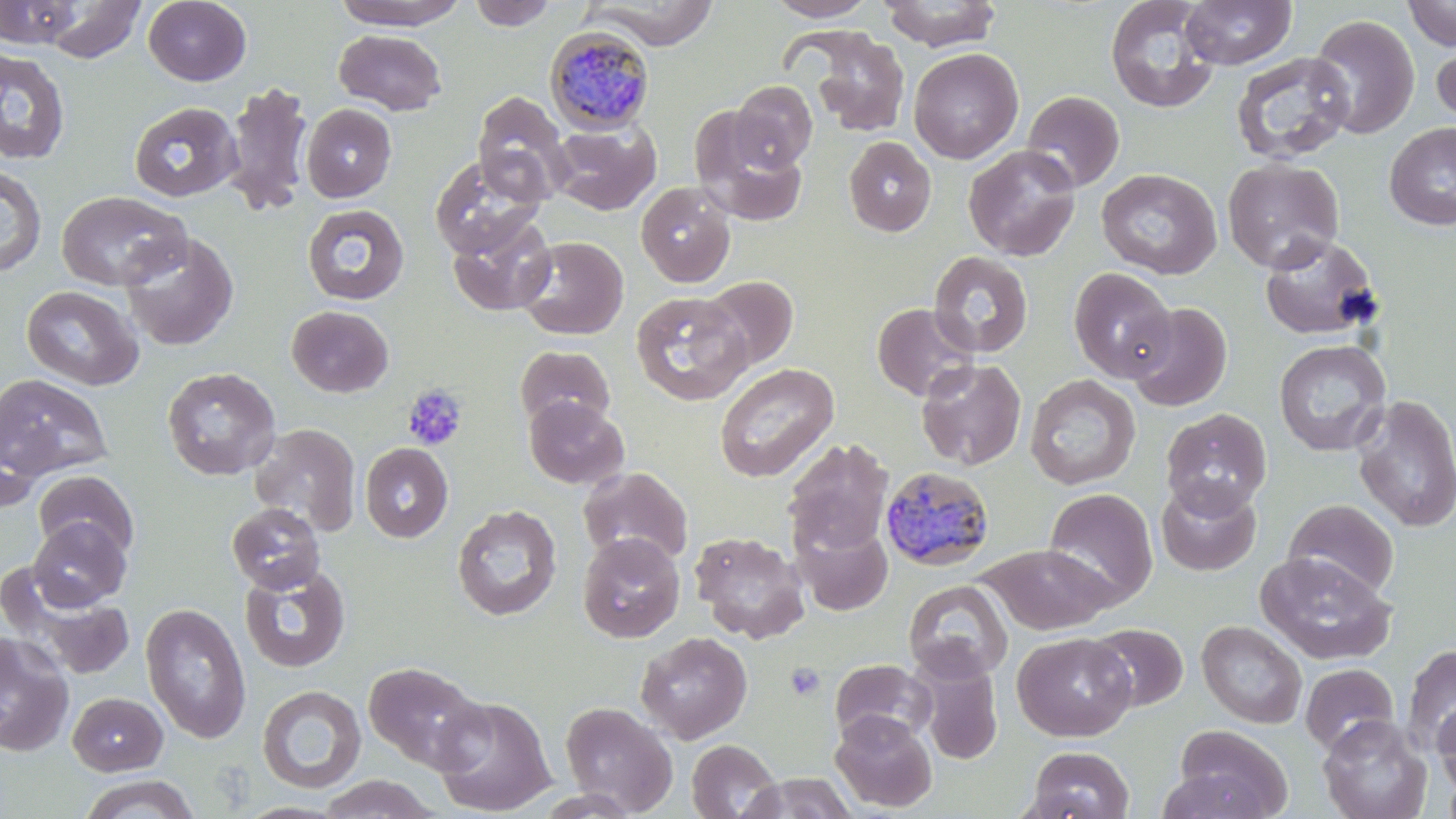
Approximate bounding boxes as [x1, y1, x2, y2] in pixels. Plasmodium malariae-infected red blood cell locations: [544, 26, 656, 134], [879, 465, 995, 571]. Platelet locations: [403, 384, 467, 450], [785, 662, 827, 701]. Uninfected red blood cell locations: [43, 0, 147, 63], [143, 0, 251, 86], [331, 0, 470, 29], [468, 0, 557, 30], [584, 0, 721, 48], [763, 0, 878, 21], [879, 0, 1003, 51], [1104, 0, 1220, 114], [1180, 0, 1296, 69], [0, 1, 84, 48], [1403, 1, 1456, 51], [1308, 14, 1420, 140], [796, 26, 912, 137], [333, 29, 447, 115], [1432, 36, 1456, 132], [0, 47, 71, 165], [909, 47, 1023, 164], [1230, 52, 1355, 165], [223, 81, 314, 216], [731, 81, 817, 171], [472, 90, 571, 203], [1021, 91, 1124, 192], [128, 101, 242, 202], [301, 103, 396, 202], [689, 108, 808, 226], [548, 122, 660, 215], [1384, 122, 1456, 230], [844, 136, 936, 237], [963, 144, 1082, 261], [429, 154, 545, 259], [1222, 158, 1344, 273], [0, 164, 47, 278], [1096, 168, 1222, 279], [635, 182, 736, 287], [56, 190, 190, 291], [302, 203, 410, 305], [446, 211, 556, 317], [120, 231, 239, 350], [1259, 232, 1381, 341], [516, 236, 628, 340], [928, 251, 1034, 358], [1068, 268, 1177, 383], [699, 276, 798, 372], [20, 285, 144, 390], [631, 291, 753, 406], [872, 302, 979, 402], [1125, 302, 1233, 412], [286, 305, 394, 398], [1273, 339, 1391, 457], [515, 345, 615, 432], [915, 358, 1026, 471], [713, 362, 839, 483], [161, 367, 281, 481], [0, 373, 113, 481], [1025, 374, 1141, 490], [1351, 395, 1456, 533], [523, 396, 629, 489], [1161, 407, 1272, 517], [0, 409, 44, 515], [249, 422, 361, 536], [783, 437, 894, 555], [361, 443, 453, 543], [578, 466, 693, 568], [33, 470, 139, 561], [1156, 479, 1261, 576], [1043, 487, 1158, 609], [1283, 499, 1399, 599], [227, 502, 326, 594], [452, 504, 562, 621], [27, 516, 131, 611], [793, 519, 893, 616], [689, 531, 809, 643], [577, 532, 685, 642], [978, 544, 1115, 634], [1254, 551, 1396, 665], [239, 564, 351, 673], [9, 578, 138, 681], [903, 579, 1013, 682], [140, 602, 251, 744], [1196, 620, 1307, 728], [1088, 623, 1188, 712], [0, 631, 74, 757], [635, 631, 753, 744], [1012, 632, 1136, 741], [1402, 643, 1456, 755], [913, 653, 1004, 764], [829, 658, 936, 747], [364, 660, 486, 772], [1300, 663, 1399, 755], [257, 684, 366, 794], [68, 690, 168, 776], [432, 696, 556, 816], [1433, 700, 1456, 797], [560, 701, 678, 816], [830, 711, 937, 812], [1318, 715, 1432, 819], [1171, 724, 1291, 819], [687, 739, 782, 819], [1026, 746, 1135, 819], [1441, 770, 1456, 819], [744, 773, 858, 818], [78, 774, 200, 818], [315, 774, 443, 818]. Slide-level diagnosis: Plasmodium malariae. 1000x magnification. Thin blood film. May-Grünwald-Giemsa stain. Single field of view. Image is 1456×819 pixels. Light microscopy.